Assess the morphology of the red blood cells.
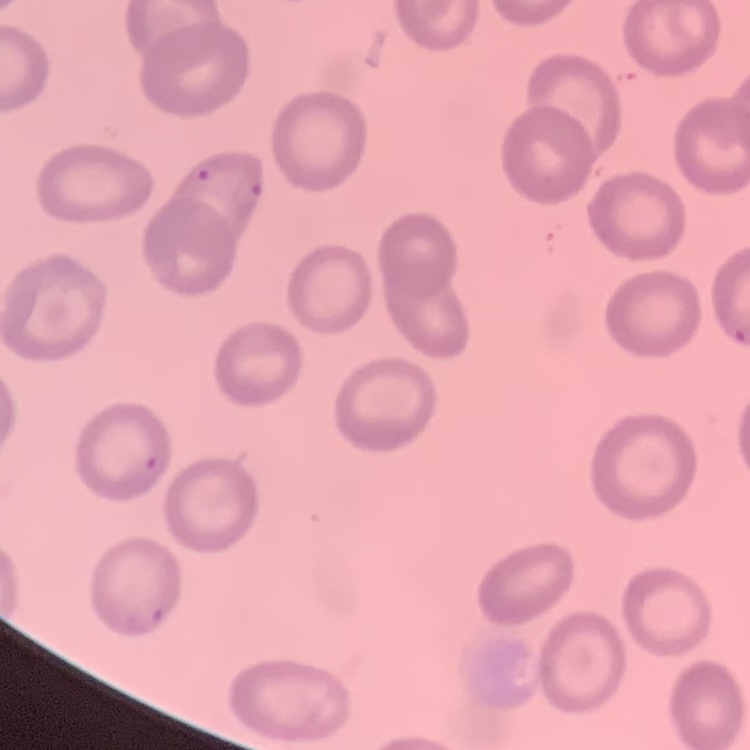
They show no rouleaux formation.

Thin blood film. Field's or Giemsa stain. One tile cut from a larger photomicrograph.